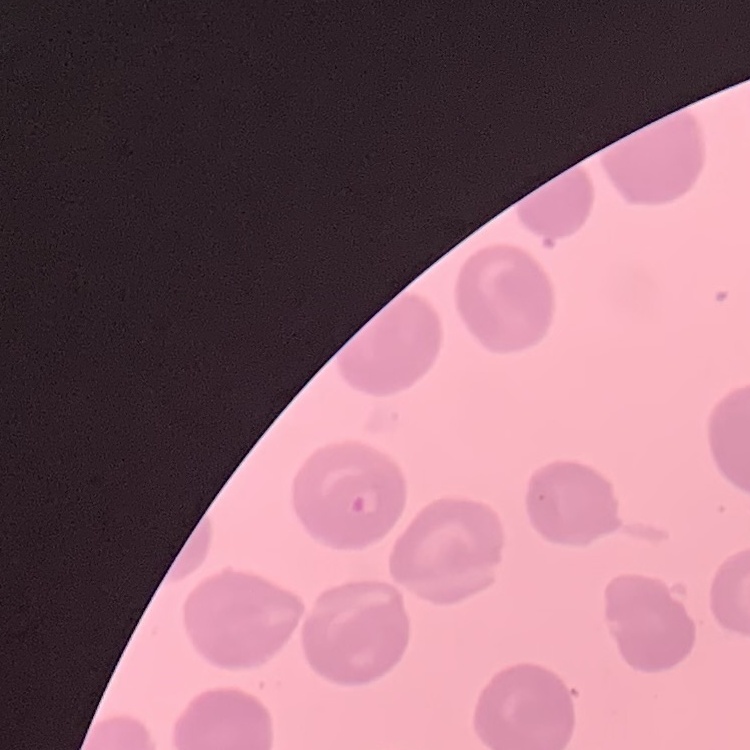
Summary:
  - Erythrocyte morphology: no rouleaux formation
  - Image type: square crop of a larger photomicrograph
  - Stain: Field's or Giemsa
  - Preparation: thin blood smear